Classify the preparation.
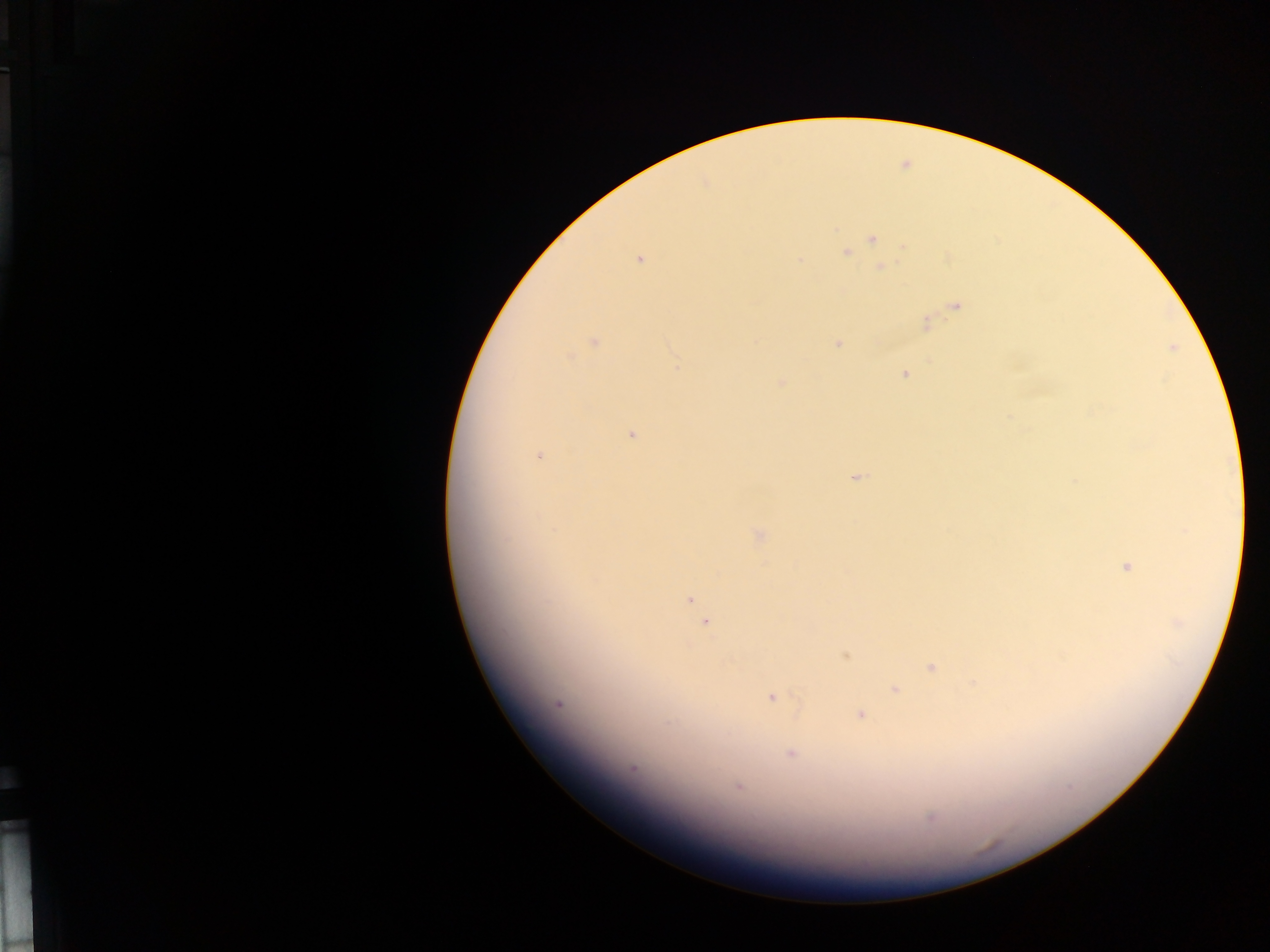
Thick blood film.

country = Ghana
field of view = single
malaria parasite locations = approximate centers as {x, y} in pixels: {871, 241}, {846, 251}, {639, 259}, {799, 260}, {926, 321}, {593, 341}, {835, 343}, {1010, 362}, {904, 374}, {781, 381}, {1009, 420}, {631, 434}, {539, 455}, {853, 479}, {756, 535}, {1124, 566}, {689, 598}, {704, 624}, {845, 657}, {929, 667}, {972, 683}, {895, 690}, {770, 697}, {560, 705}, {861, 715}, {790, 753}, {633, 768}, {738, 787}, {929, 818}
image size = 1270×952 pixels
capture = mobile-phone photograph through a microscope